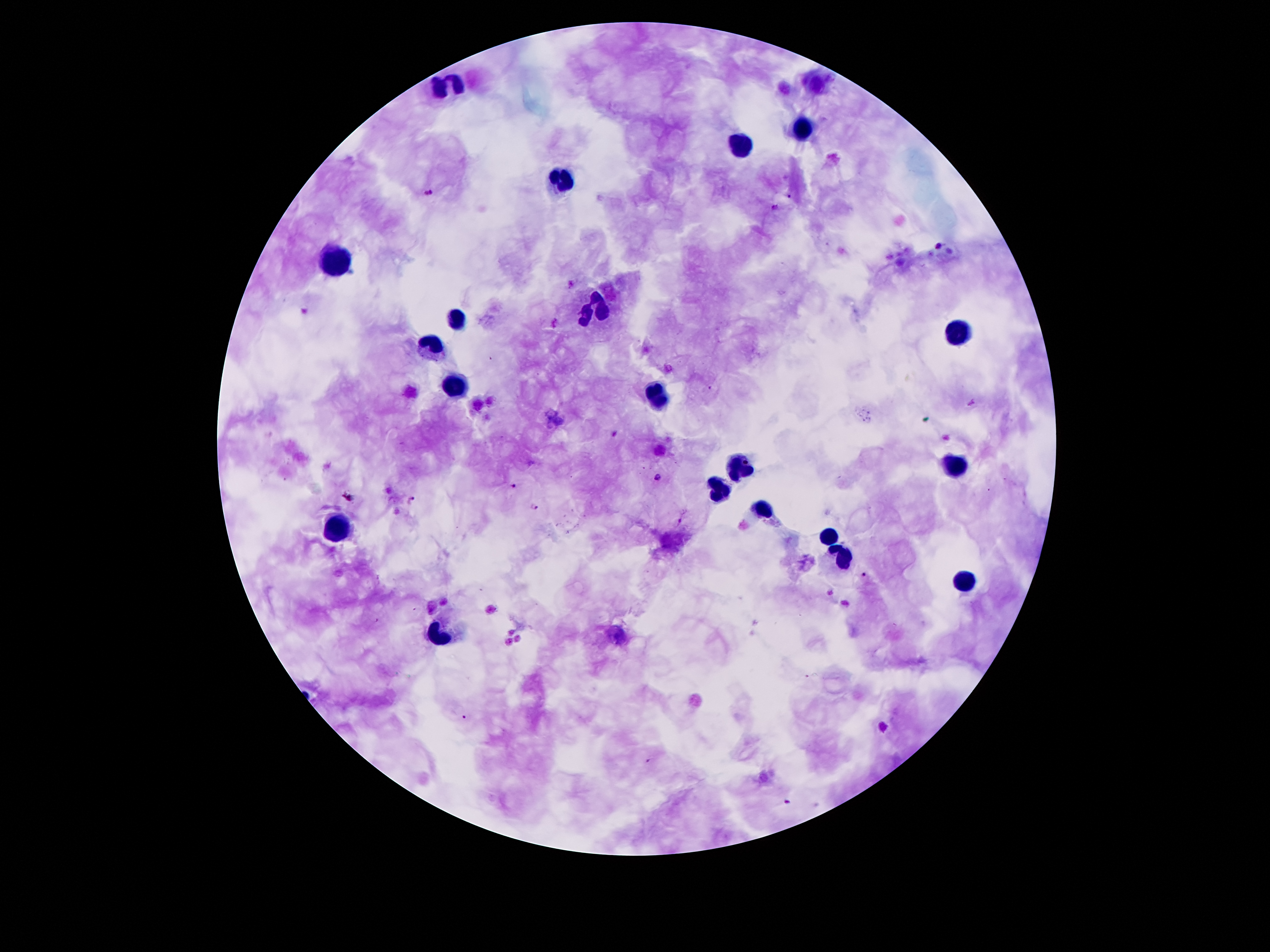
Approximate object centers, in pixels from the top-left corner.
Summary:
  - Malaria parasite locations: (x=430, y=193), (x=790, y=196), (x=775, y=208), (x=939, y=246), (x=658, y=478), (x=515, y=485), (x=411, y=501), (x=536, y=507), (x=862, y=578), (x=463, y=717), (x=648, y=761), (x=790, y=802)
  - Leukocyte locations: (x=446, y=83), (x=803, y=127), (x=740, y=148), (x=556, y=180), (x=341, y=261), (x=596, y=304), (x=455, y=320), (x=957, y=335), (x=430, y=349), (x=455, y=389), (x=656, y=398), (x=740, y=467), (x=956, y=467), (x=719, y=490), (x=763, y=509), (x=339, y=527), (x=826, y=533), (x=845, y=557), (x=965, y=585), (x=440, y=634)
  - Field of view: one from this slide
  - Magnification: 100x
  - Image size: 1270×952 pixels
  - Preparation: thick peripheral-blood smear
  - Stain: Giemsa
  - Capture: smartphone through the microscope eyepiece
  - Patient malaria status: positive for Plasmodium falciparum